Identify the parasite.
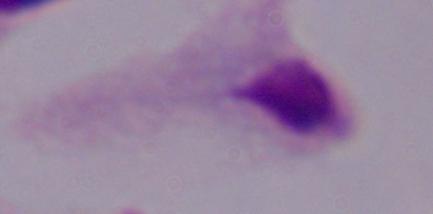
A trichomonad.

Captured at 1000x magnification. Photomicrograph.